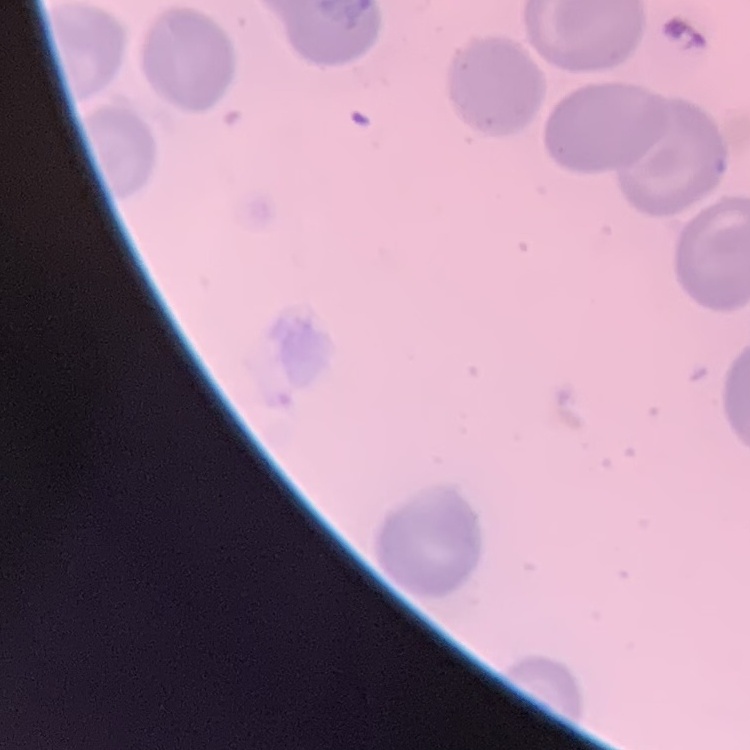

Summary:
  - Red blood cell morphology: no rouleaux formation
  - Stain: Field's or Giemsa
  - Preparation: thin blood smear
  - Image type: one tile cut from a larger photomicrograph